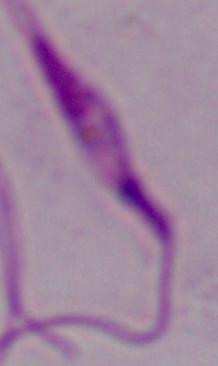
magnification: 1000x
identification: Leishmania
modality: micrograph